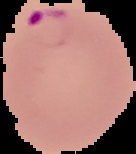
Result: Plasmodium parasites identified. Image is 136×154 pixels. The area outside the segmented cell region is set to black. From a thin blood smear.